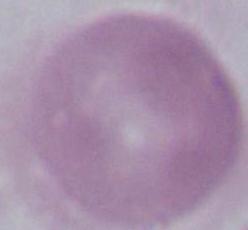
magnification: 1000x
identification: red blood cell
modality: photomicrograph